State which parasite is depicted.
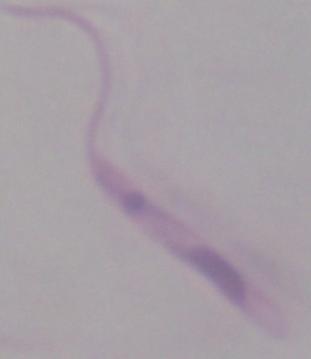
Leishmania.

modality = micrograph
magnification = 1000x